Comment on the morphology of the erythrocytes.
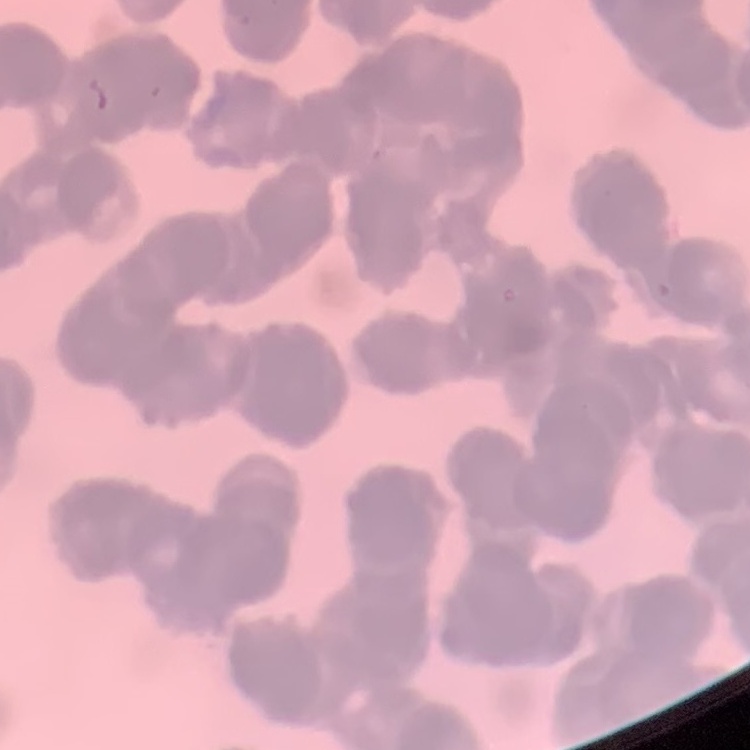
Rouleaux formation.

Summary:
  - Preparation: thin peripheral smear
  - Stain: Field's or Giemsa
  - Image type: one tile cut from a larger photomicrograph